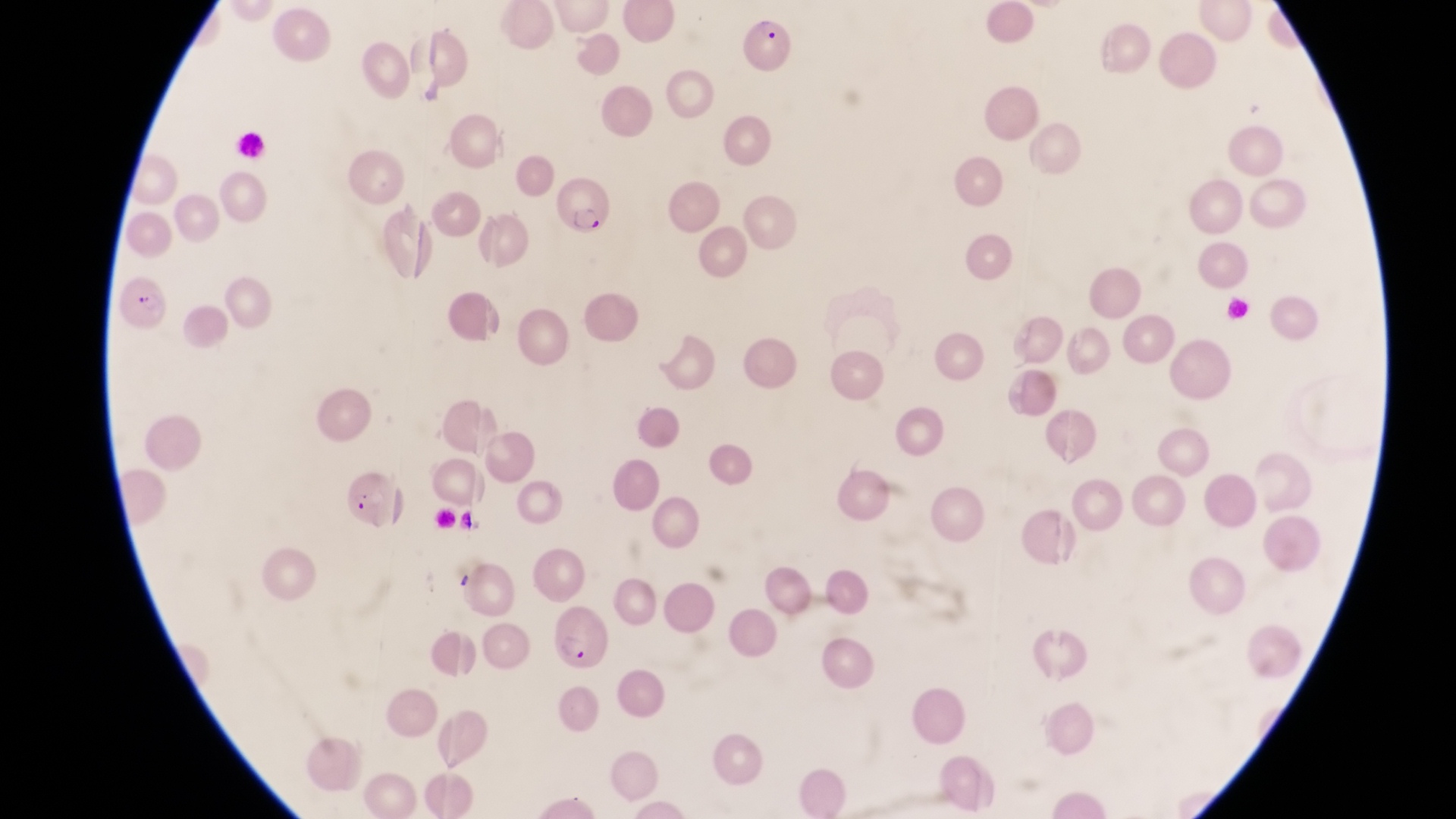
Approximate bounding boxes as [left, top, right, bottom] in pixels. Parasitised red blood cell locations: [746, 17, 796, 80], [554, 180, 614, 238], [118, 272, 171, 332], [555, 605, 615, 674]. Image is 1456×819 pixels. Photographed through the eyepiece of an Olympus CX-23 microscope with a smartphone camera. Magnification of 1000x. Thin blood film. Collected in Uganda. Single field of view.